Locate and identify every blood parasite.
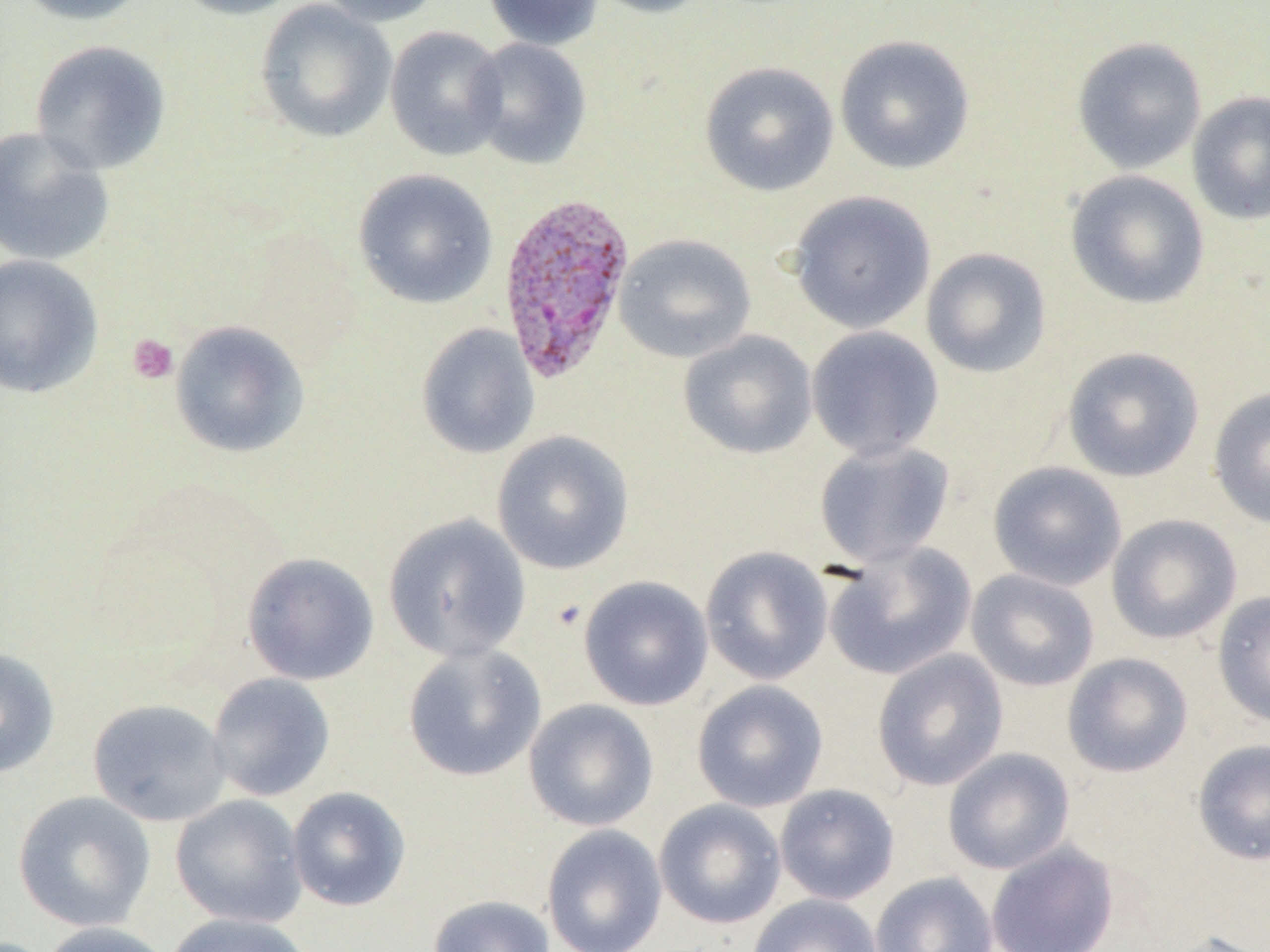

Approximate bounding boxes as named x1/y1/x2/y2 corners in pixels.
Plasmodium vivax-infected red blood cells: (x1=497, y1=191, x2=638, y2=387).
No Plasmodium falciparum, Plasmodium ovale, Plasmodium malariae, Babesia divergens, or Trypanosoma brucei observed.

Summary:
  - Platelet locations: (x1=127, y1=333, x2=179, y2=385)
  - Uninfected red blood cell locations: (x1=12, y1=0, x2=154, y2=26), (x1=169, y1=0, x2=308, y2=20), (x1=254, y1=0, x2=397, y2=144), (x1=315, y1=0, x2=442, y2=27), (x1=482, y1=0, x2=605, y2=50), (x1=586, y1=0, x2=715, y2=18), (x1=384, y1=26, x2=509, y2=161), (x1=834, y1=35, x2=976, y2=175), (x1=467, y1=37, x2=592, y2=169), (x1=1071, y1=37, x2=1207, y2=174), (x1=29, y1=40, x2=172, y2=175), (x1=699, y1=61, x2=839, y2=197), (x1=1187, y1=91, x2=1270, y2=226), (x1=0, y1=126, x2=116, y2=267), (x1=352, y1=169, x2=498, y2=310), (x1=1065, y1=169, x2=1210, y2=310), (x1=788, y1=191, x2=936, y2=334), (x1=614, y1=233, x2=756, y2=363), (x1=920, y1=247, x2=1052, y2=378), (x1=0, y1=254, x2=103, y2=398), (x1=169, y1=320, x2=310, y2=458), (x1=416, y1=323, x2=540, y2=459), (x1=805, y1=325, x2=945, y2=461), (x1=678, y1=329, x2=818, y2=459), (x1=1061, y1=346, x2=1205, y2=482), (x1=1208, y1=387, x2=1270, y2=529), (x1=491, y1=430, x2=635, y2=575), (x1=813, y1=440, x2=955, y2=568), (x1=987, y1=461, x2=1127, y2=591), (x1=382, y1=513, x2=531, y2=664), (x1=1106, y1=514, x2=1242, y2=644), (x1=823, y1=542, x2=978, y2=680), (x1=699, y1=546, x2=834, y2=685), (x1=241, y1=552, x2=380, y2=685), (x1=965, y1=568, x2=1100, y2=691), (x1=578, y1=575, x2=714, y2=711), (x1=1212, y1=590, x2=1270, y2=728), (x1=402, y1=643, x2=546, y2=782), (x1=0, y1=646, x2=60, y2=778), (x1=872, y1=649, x2=1009, y2=791), (x1=1062, y1=652, x2=1193, y2=778), (x1=207, y1=672, x2=336, y2=802), (x1=691, y1=680, x2=829, y2=812), (x1=87, y1=698, x2=232, y2=827), (x1=524, y1=698, x2=659, y2=831), (x1=1191, y1=739, x2=1270, y2=866), (x1=942, y1=747, x2=1075, y2=874), (x1=774, y1=783, x2=900, y2=905), (x1=286, y1=786, x2=411, y2=911), (x1=13, y1=790, x2=156, y2=932), (x1=170, y1=794, x2=309, y2=929), (x1=653, y1=799, x2=787, y2=929), (x1=541, y1=824, x2=667, y2=952), (x1=986, y1=841, x2=1119, y2=952), (x1=870, y1=871, x2=998, y2=952), (x1=427, y1=894, x2=556, y2=952), (x1=747, y1=894, x2=885, y2=952), (x1=165, y1=912, x2=313, y2=952), (x1=38, y1=921, x2=173, y2=952), (x1=1158, y1=930, x2=1270, y2=952)
  - Slide-level diagnosis: Plasmodium vivax
  - Image size: 1270×952 pixels
  - Field of view: single
  - Magnification: 1000x
  - Preparation: thin blood film
  - Modality: optical microscopy